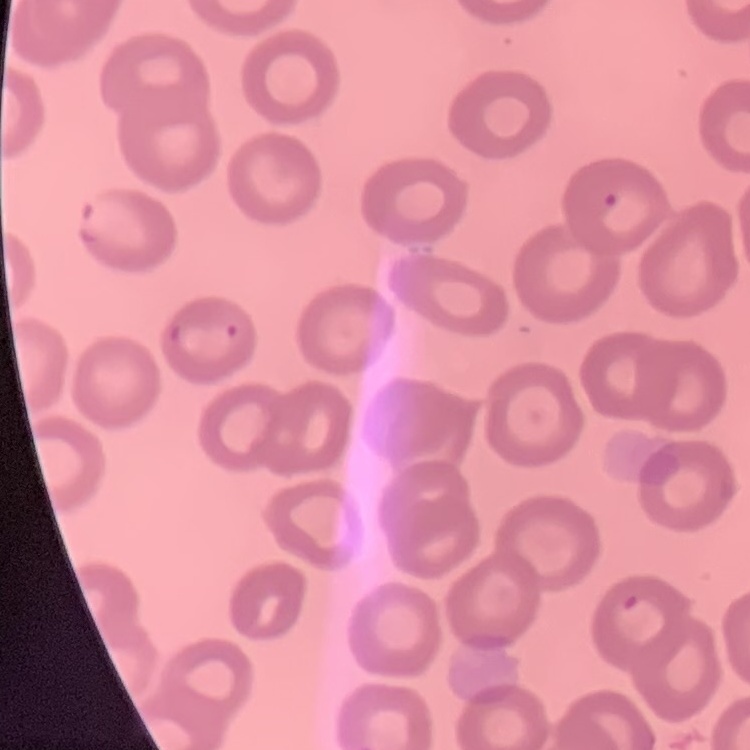
red_blood_cell_morphology: no rouleaux formation
image_type: square crop of a larger photomicrograph
preparation: thin blood smear
stain: Field's or Giemsa